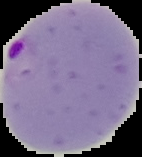

image_type: segmented cell region with the area outside set to black
image_size: 142×157 pixels
result: Plasmodium parasites detected
preparation: thin blood film